Give the position of every Plasmodium parasite visible.
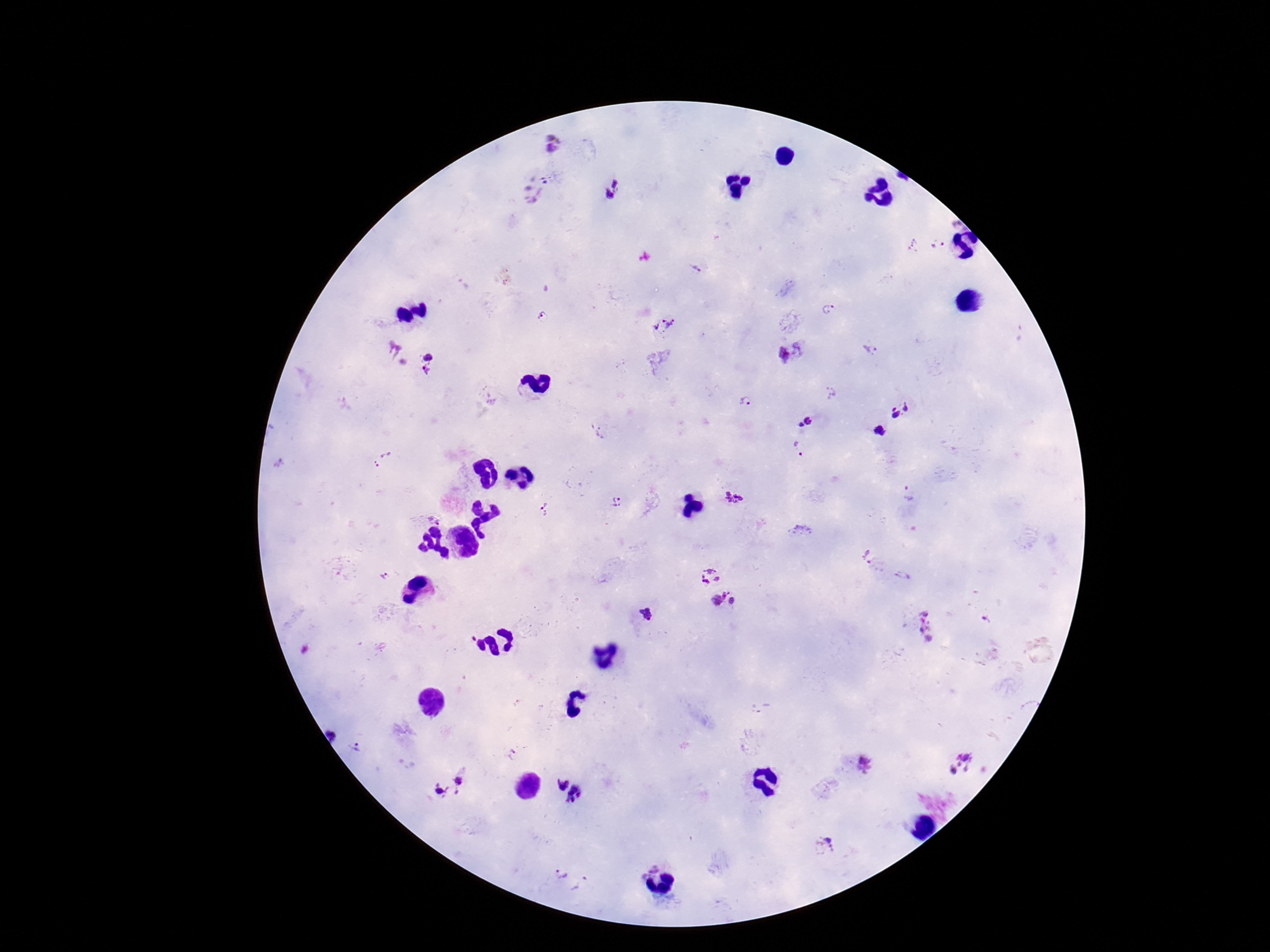

Approximate centers as {x, y} in pixels.
Plasmodium parasites: {551, 142}, {535, 186}, {614, 188}, {939, 246}, {913, 247}, {696, 267}, {827, 309}, {664, 325}, {398, 354}, {789, 354}, {429, 364}, {748, 401}, {902, 409}, {806, 422}, {881, 428}, {597, 432}, {799, 448}, {384, 460}, {734, 499}, {617, 501}, {545, 510}, {800, 531}, {862, 555}, {901, 575}, {711, 576}, {724, 602}, {648, 615}, {928, 631}, {360, 750}, {514, 756}, {961, 764}, {868, 766}, {461, 780}, {442, 796}, {826, 847}, {558, 877}, {585, 886}.

magnification = 100x
image size = 1270×952 pixels
preparation = thick peripheral-blood smear
patient malaria status = infected
field of view = one from this slide
capture = smartphone camera through the microscope eyepiece
stain = Giemsa